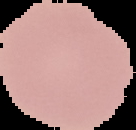

malaria status = uninfected
image size = 136×130 pixels
image type = segmented cell region on a black background
preparation = thin blood smear